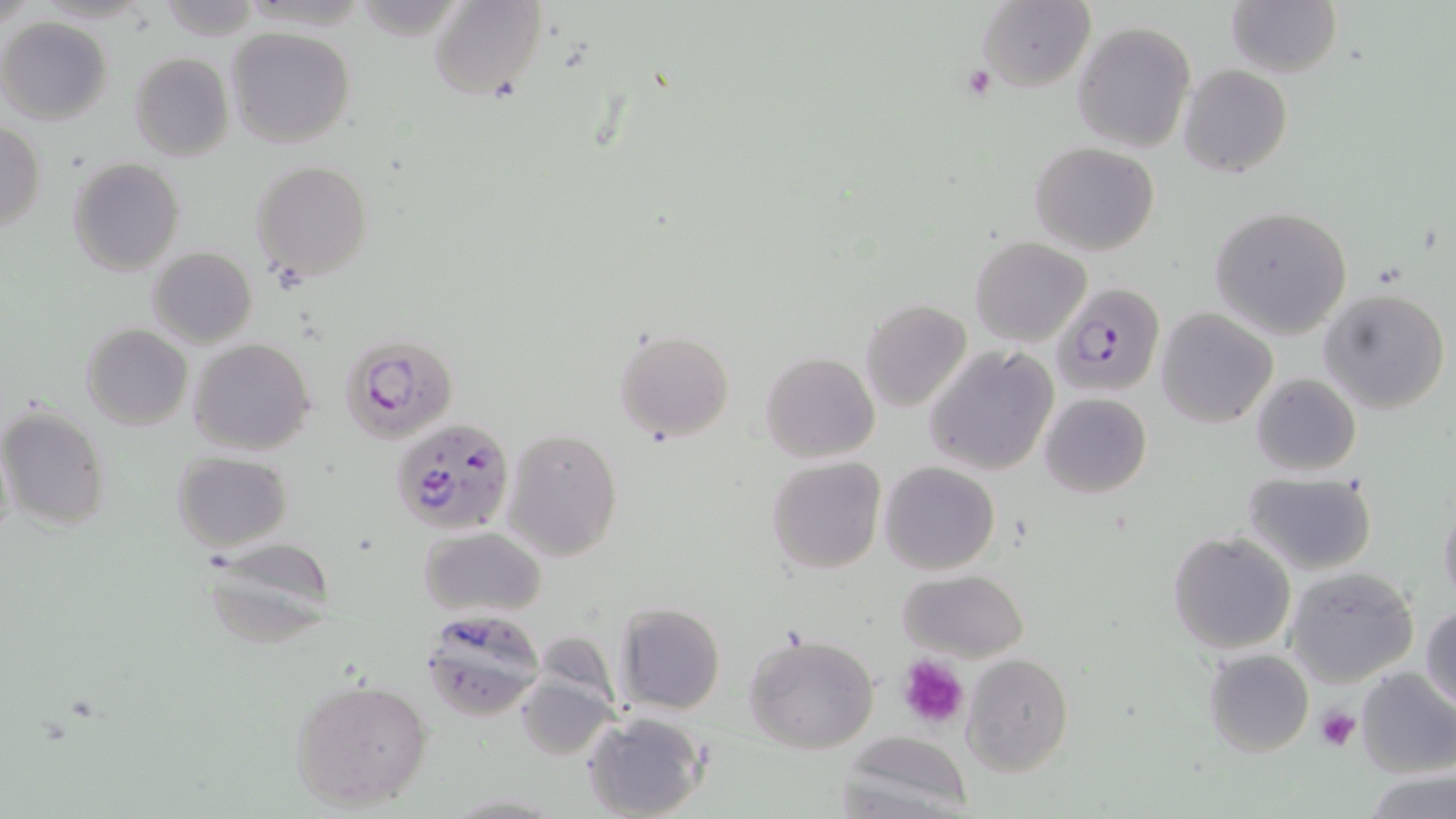

{
  "slide_level_diagnosis": "Plasmodium falciparum",
  "preparation": "thin blood smear",
  "platelet_locations": "approximate bounding boxes as [x1, y1, x2, y2] in pixels: [960, 62, 996, 103], [896, 655, 970, 730], [1315, 707, 1361, 752]",
  "stain": "May-Grünwald-Giemsa",
  "uninfected_red_blood_cell_locations": "approximate bounding boxes as [x1, y1, x2, y2] in pixels: [429, 0, 546, 101], [976, 1, 1096, 91], [1226, 1, 1341, 80], [154, 4, 263, 37], [1, 17, 113, 125], [1072, 21, 1196, 153], [227, 26, 355, 149], [130, 53, 233, 162], [1178, 65, 1294, 178], [0, 121, 46, 232], [1031, 141, 1160, 256], [67, 157, 184, 276], [251, 161, 374, 283], [1211, 206, 1352, 339], [971, 236, 1090, 345], [147, 246, 258, 348], [1319, 287, 1452, 413], [861, 299, 972, 414], [882, 307, 1011, 452], [1156, 309, 1276, 427], [82, 324, 193, 431], [613, 329, 735, 444], [189, 338, 315, 456], [924, 344, 1060, 476], [759, 352, 880, 463], [1250, 373, 1361, 478], [1039, 393, 1152, 498], [0, 404, 111, 532], [502, 426, 624, 562], [1, 431, 15, 550], [171, 453, 292, 551], [767, 457, 886, 574], [879, 461, 1000, 575], [1242, 471, 1380, 576], [1439, 495, 1456, 612], [418, 526, 547, 618], [1167, 531, 1297, 655], [197, 540, 338, 649], [1284, 566, 1420, 687], [897, 569, 1028, 662], [614, 602, 726, 716], [1422, 604, 1456, 713], [421, 610, 545, 719], [743, 634, 879, 755], [1202, 648, 1314, 757], [960, 653, 1074, 776], [1354, 666, 1456, 777], [288, 676, 435, 814], [514, 676, 617, 761], [581, 711, 709, 819], [837, 733, 972, 819], [1365, 770, 1455, 819]",
  "modality": "optical microscopy",
  "plasmodium_falciparum_infected_red_blood_cell_locations": "approximate bounding boxes as [x1, y1, x2, y2] in pixels: [1052, 284, 1163, 397], [336, 334, 459, 445], [392, 417, 515, 537]",
  "magnification": "1000x",
  "image_size": "1456×819 pixels",
  "field_of_view": "one of a larger specimen"
}